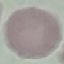

{
  "result": "no malaria parasites seen",
  "capture": "smartphone through the microscope eyepiece",
  "stain": "Giemsa",
  "image_type": "cell patch, automatically extracted from a larger field of view and resized to 64 × 64 pixels",
  "preparation": "thin blood smear"
}